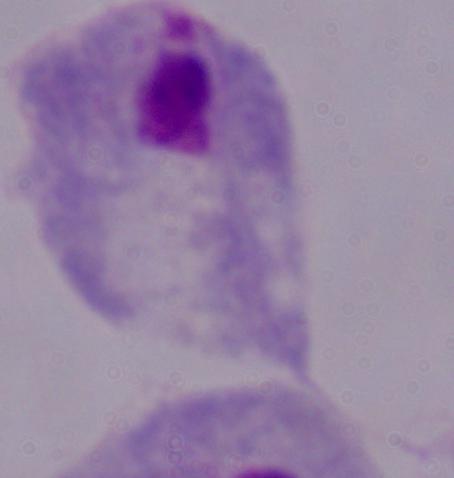

identification = trichomonad
modality = photomicrograph
magnification = 1000x